Give the extent of all Plasmodium falciparum-infected red blood cells.
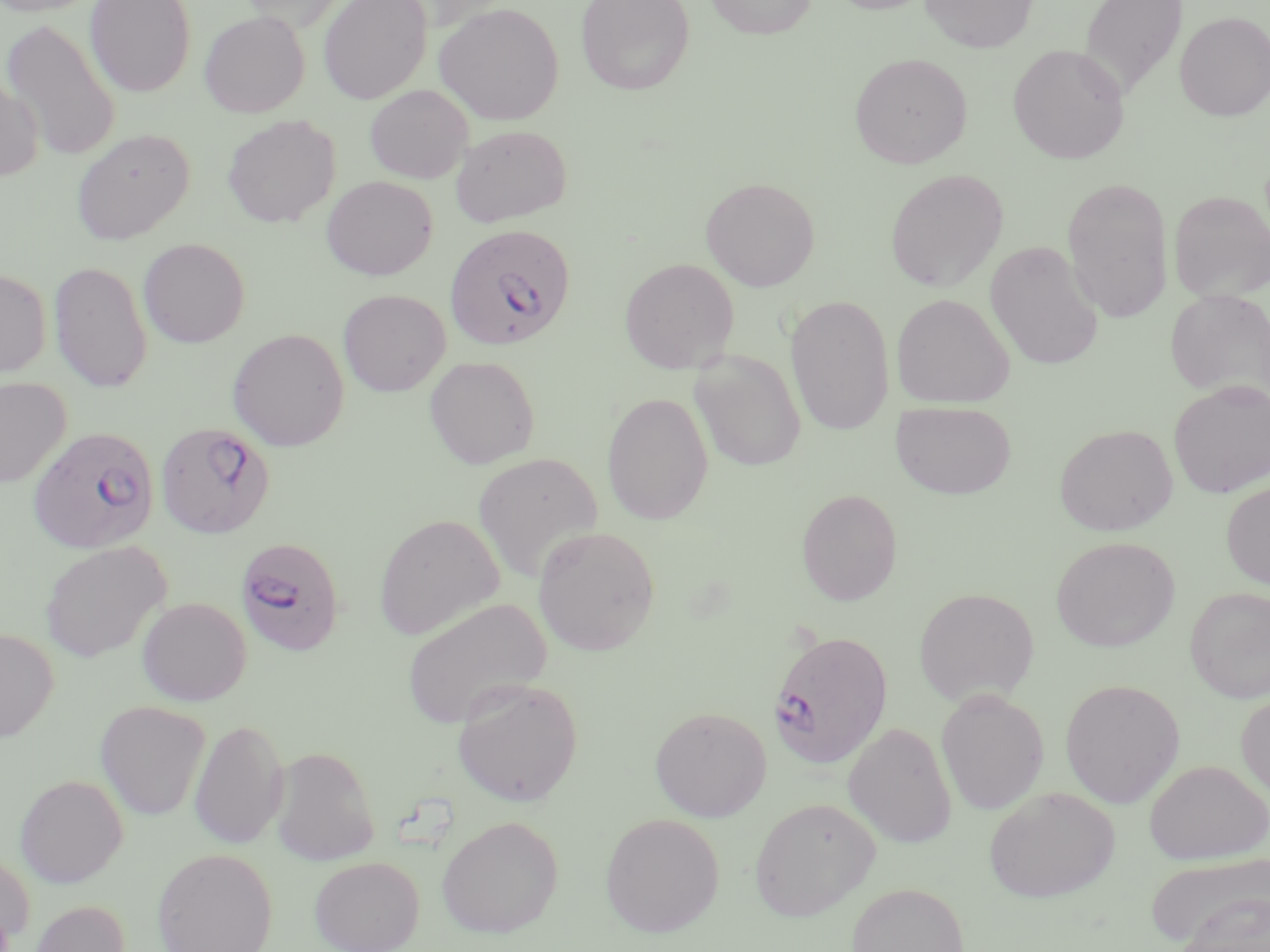
Approximate bounding boxes as (x1,y1)-(x2,y2) corner pairs in pixels.
Plasmodium falciparum-infected red blood cells: (444,223)-(575,351), (155,421)-(275,539), (27,425)-(160,554), (235,536)-(345,656), (767,628)-(893,770).

Uninfected red blood cell locations: (0,0)-(103,17), (85,0)-(196,97), (240,0)-(351,32), (318,0)-(432,104), (575,0)-(695,96), (704,0)-(818,39), (825,0)-(938,15), (920,0)-(1038,53), (1078,0)-(1188,101), (434,2)-(564,126), (199,11)-(310,118), (1175,12)-(1270,121), (1,17)-(122,163), (1008,44)-(1130,164), (850,52)-(973,168), (0,73)-(43,182), (365,85)-(473,184), (222,114)-(340,228), (451,124)-(571,226), (71,128)-(194,244), (885,168)-(1009,292), (321,175)-(438,280), (701,177)-(820,291), (1062,177)-(1174,322), (1169,191)-(1270,303), (138,237)-(250,348), (985,240)-(1105,371), (619,257)-(740,373), (49,260)-(152,393), (0,267)-(51,380), (338,289)-(450,397), (1166,289)-(1270,404), (891,293)-(1014,407), (785,294)-(895,435), (227,328)-(349,451), (690,349)-(806,472), (424,355)-(540,469), (0,378)-(71,488), (1168,379)-(1270,498), (602,392)-(714,525), (890,400)-(1017,499), (1054,423)-(1178,535), (472,451)-(604,583), (1221,480)-(1270,590), (796,488)-(903,606), (374,513)-(504,641), (532,525)-(660,656), (1051,536)-(1179,652), (39,541)-(172,662), (1185,586)-(1270,703), (913,587)-(1040,706), (136,596)-(251,706), (401,596)-(551,730), (0,628)-(59,742), (452,678)-(584,807), (1060,678)-(1185,808), (936,689)-(1049,815), (1236,690)-(1270,801), (95,701)-(210,821), (649,706)-(772,822), (189,717)-(289,850), (843,721)-(957,848), (270,746)-(380,866), (1144,759)-(1269,864), (15,774)-(128,888), (984,787)-(1119,902), (749,796)-(881,920), (600,812)-(724,937), (435,814)-(564,938), (153,848)-(278,952), (0,851)-(35,947), (1146,853)-(1270,950), (310,856)-(424,952), (846,882)-(970,952), (1180,895)-(1269,952), (27,899)-(130,952). Slide-level diagnosis: Plasmodium falciparum. Single field of view. Captured at 1000x magnification. Thin blood film. May-Grünwald-Giemsa stain. Optical microscopy. Image is 1270×952 pixels.